Assess the morphology of the red blood cells.
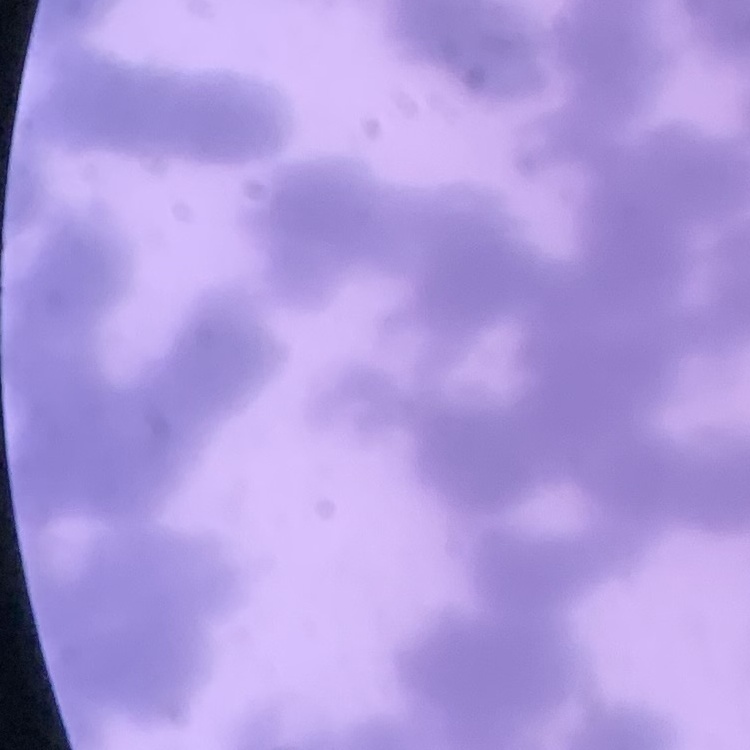
They show rouleaux formation.

Summary:
  - Preparation: thin blood smear
  - Image type: one tile cut from a larger photomicrograph
  - Stain: Field's or Giemsa